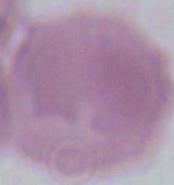
identification: red blood cell
magnification: 1000x
modality: photomicrograph